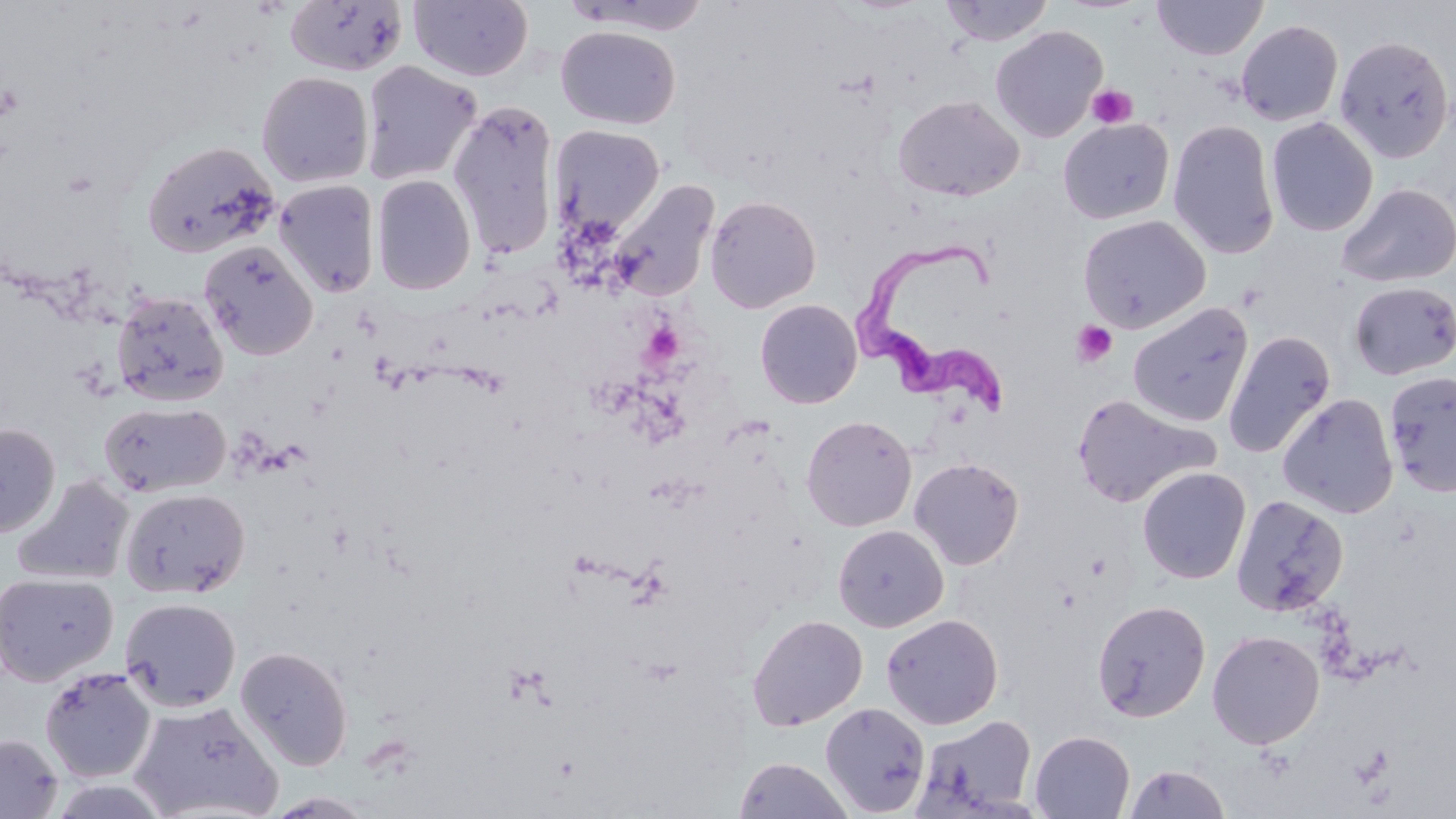
slide_level_diagnosis: Trypanosoma brucei
modality: light microscopy
trypanosoma_brucei_locations: 'approximate bounding boxes as (x1,y1)-(x2,y2) corner pairs in pixels: (847,234)-(1020,422)'
image_size: 1456×819 pixels
platelet_locations: 'approximate bounding boxes as (x1,y1)-(x2,y2) corner pairs in pixels: (0,82)-(22,123), (1086,84)-(1138,129), (1072,321)-(1118,366), (642,323)-(684,366)'
field_of_view: one of a larger specimen
stain: May-Grünwald-Giemsa
uninfected_red_blood_cell_locations: 'approximate bounding boxes as (x1,y1)-(x2,y2) corner pairs in pixels: (284,0)-(409,77), (409,0)-(533,82), (940,0)-(1055,46), (1152,0)-(1268,60), (1235,19)-(1344,126), (990,25)-(1108,142), (556,26)-(680,130), (1334,35)-(1455,163), (360,60)-(482,186), (256,71)-(374,188), (893,95)-(1025,202), (449,100)-(561,261), (1058,117)-(1174,224), (1266,117)-(1378,237), (1167,119)-(1280,259), (550,124)-(666,238), (140,140)-(280,260), (371,174)-(477,296), (273,179)-(381,297), (608,179)-(719,302), (1337,182)-(1455,288), (704,195)-(821,313), (1077,214)-(1211,333), (199,240)-(319,360), (1348,281)-(1456,380), (111,290)-(229,407), (754,299)-(862,409), (1127,301)-(1254,428), (1222,330)-(1336,459), (1383,370)-(1456,497), (1277,393)-(1399,519), (1071,394)-(1219,509), (99,400)-(231,498), (801,415)-(917,532), (0,424)-(60,538), (909,457)-(1024,570), (1137,466)-(1251,584), (12,474)-(135,586), (119,487)-(250,599), (1231,494)-(1349,616), (832,524)-(949,632), (0,571)-(118,686), (119,597)-(241,712), (1091,599)-(1211,723), (881,613)-(1004,729), (747,614)-(868,731), (1207,630)-(1325,749), (235,645)-(353,771), (39,666)-(157,783), (129,699)-(283,819), (820,702)-(930,816), (913,714)-(1038,815), (1029,730)-(1135,818), (0,733)-(63,819), (734,757)-(852,818), (1122,763)-(1231,819), (265,791)-(377,818)'
magnification: 1000x
preparation: thin blood film